Point out each leukocyte.
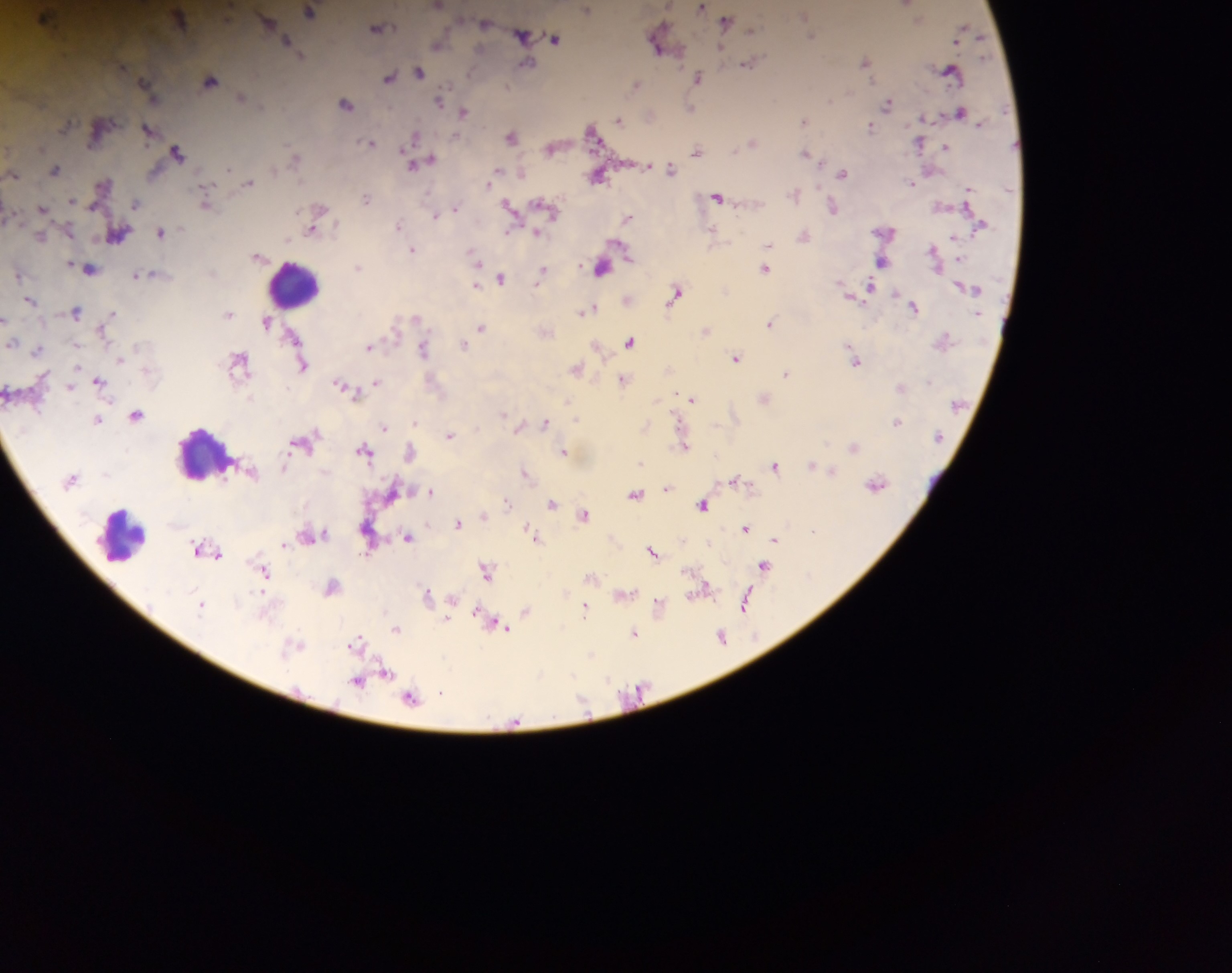

Approximate centers as {x, y} in pixels.
Leukocytes: {296, 285}, {208, 454}, {121, 534}.

Summary:
  - Plasmodium parasite locations: {906, 4}, {439, 5}, {702, 7}, {586, 9}, {310, 11}, {45, 15}, {805, 15}, {179, 17}, {918, 20}, {266, 21}, {726, 21}, {485, 23}, {378, 27}, {963, 31}, {522, 32}, {810, 35}, {556, 38}, {286, 40}, {658, 41}, {439, 45}, {865, 61}, {749, 62}, {526, 63}, {419, 71}, {951, 71}, {699, 76}, {390, 77}, {210, 80}, {636, 84}, {242, 97}, {830, 99}, {440, 100}, {888, 103}, {345, 104}, {690, 108}, {464, 111}, {961, 112}, {619, 119}, {803, 120}, {871, 127}, {147, 130}, {592, 132}, {512, 136}, {414, 137}, {918, 141}, {370, 142}, {753, 142}, {946, 147}, {551, 148}, {697, 149}, {177, 152}, {807, 154}, {296, 157}, {422, 162}, {413, 164}, {55, 168}, {670, 168}, {228, 170}, {843, 172}, {14, 174}, {492, 176}, {597, 176}, {249, 181}, {911, 181}, {103, 183}, {794, 194}, {718, 196}, {366, 198}, {207, 201}, {137, 203}, {546, 206}, {833, 206}, {511, 207}, {43, 208}, {455, 208}, {438, 213}, {627, 217}, {399, 224}, {314, 227}, {162, 231}, {713, 232}, {118, 235}, {804, 235}, {41, 236}, {769, 245}, {413, 250}, {933, 251}, {256, 256}, {475, 257}, {882, 261}, {358, 266}, {90, 268}, {602, 268}, {764, 268}, {542, 272}, {140, 274}, {501, 277}, {475, 285}, {868, 286}, {676, 292}, {895, 293}, {30, 300}, {915, 306}, {587, 310}, {76, 311}, {229, 313}, {110, 314}, {417, 318}, {4, 319}, {267, 322}, {770, 323}, {482, 327}, {707, 329}, {294, 335}, {944, 339}, {630, 342}, {12, 343}, {463, 345}, {370, 346}, {38, 348}, {423, 349}, {736, 357}, {240, 360}, {856, 360}, {303, 365}, {577, 368}, {786, 372}, {623, 379}, {376, 380}, {99, 381}, {341, 385}, {901, 387}, {692, 398}, {764, 398}, {136, 414}, {503, 414}, {97, 419}, {415, 421}, {897, 421}, {545, 422}, {385, 427}, {450, 434}, {684, 444}, {854, 445}, {365, 449}, {410, 451}, {564, 451}, {813, 464}, {285, 465}, {775, 465}, {832, 470}, {525, 472}, {736, 479}, {876, 483}, {668, 486}, {431, 491}, {636, 493}, {507, 501}, {553, 503}, {702, 504}, {585, 514}, {483, 515}, {458, 522}, {746, 527}, {313, 534}, {407, 534}, {533, 534}, {775, 539}, {285, 543}, {196, 546}, {653, 551}, {218, 553}, {764, 565}, {486, 569}, {264, 571}, {591, 576}, {332, 585}, {705, 588}, {427, 593}, {625, 593}, {452, 601}, {201, 604}, {745, 604}, {658, 605}, {586, 608}, {527, 611}, {482, 615}, {448, 620}, {500, 626}, {396, 628}, {633, 632}, {722, 636}, {357, 641}, {296, 645}, {591, 653}, {386, 672}, {358, 680}, {441, 691}, {411, 697}
  - Image size: 1232×973 pixels
  - Capture: mobile-phone photograph through a microscope
  - Country: Ghana
  - Preparation: thick blood smear
  - Field of view: single